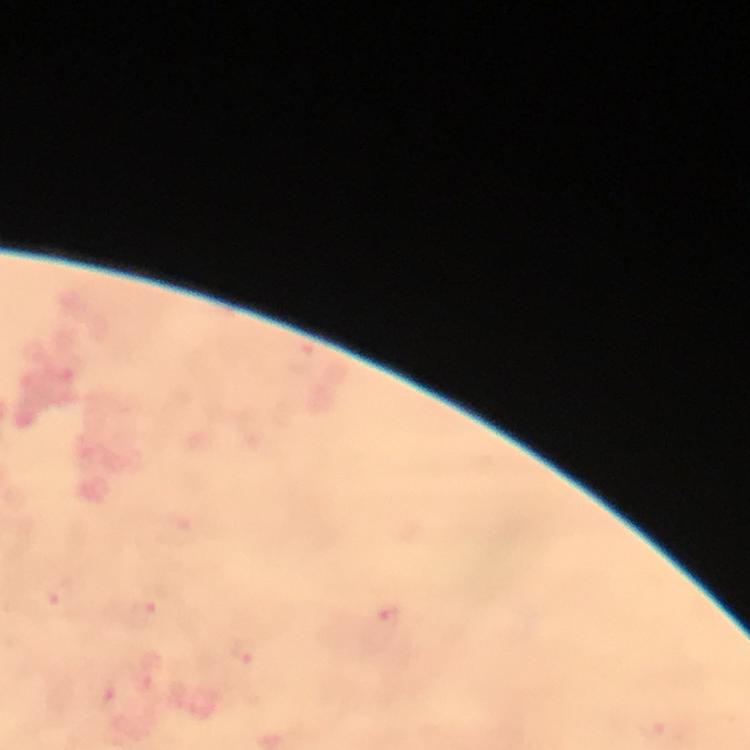

stain = Giemsa
malaria parasite locations = approximate object centers, in pixels from the top-left corner: (x=63, y=593), (x=145, y=611), (x=389, y=618), (x=246, y=651), (x=654, y=729)
preparation = thick smear
magnification = 100x
cropped from = one field of view
immersion oil = applied
image size = 750×750 pixels
context = from a malaria diagnostic workup
capture = smartphone camera through the microscope